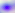

Photomicrograph. 400x magnification. Toxoplasma gondii is shown.